Name the parasite shown.
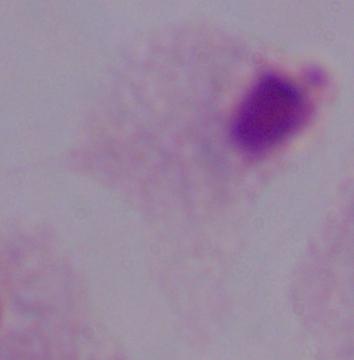

A trichomonad.

Summary:
  - Magnification: 1000x
  - Modality: photomicrograph